Assess this cell for malaria.
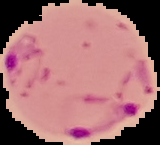

Parasitized.

Summary:
  - Preparation: thin blood smear
  - Image size: 160×145 pixels
  - Image type: cell region segmented out of the field of view; surrounding area masked to black